Outline each uninfected red blood cell.
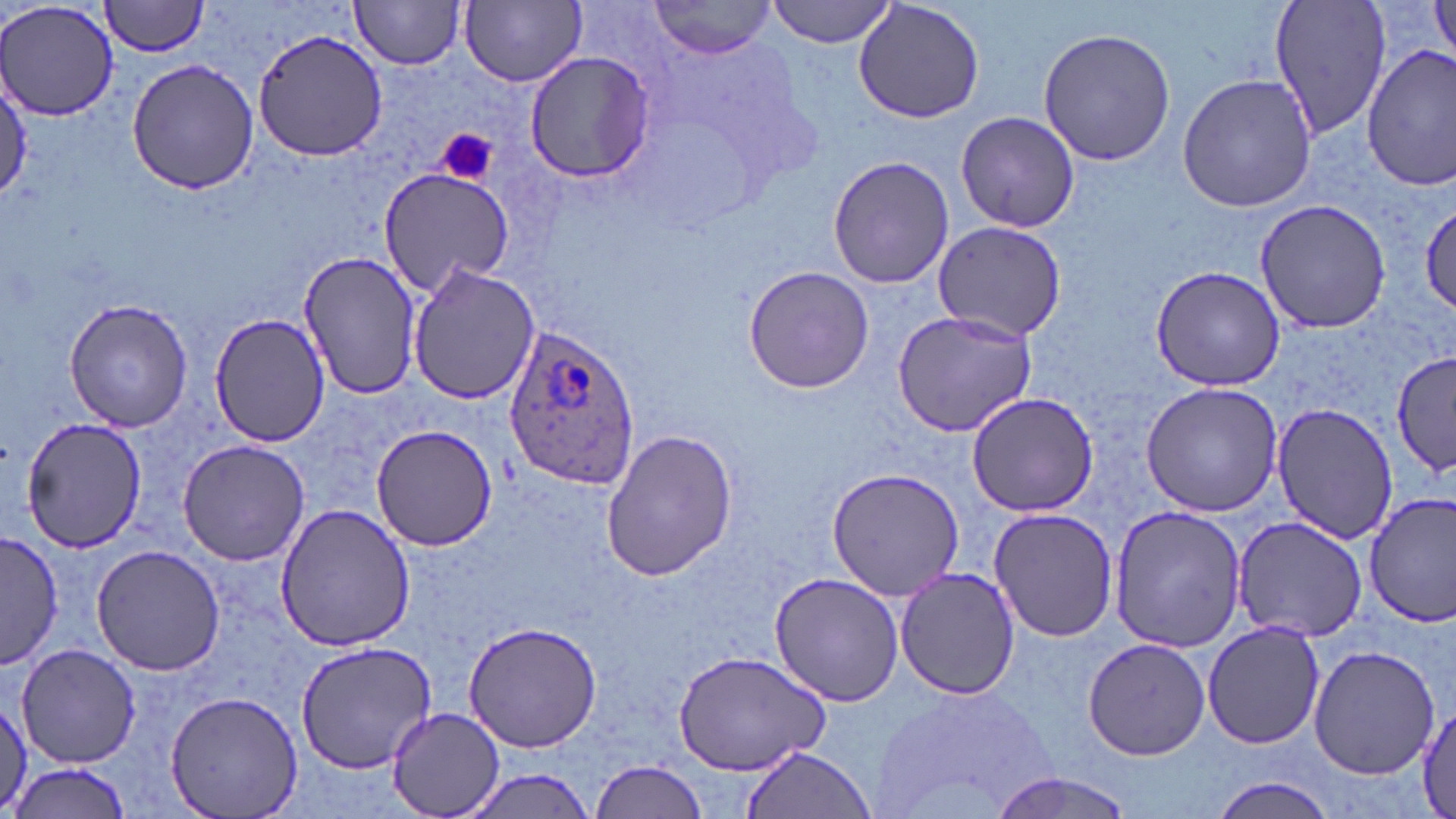
Approximate bounding boxes as (x1,y1)-(x2,y2) corner pairs in pixels.
Uninfected red blood cells: (100,0)-(213,57), (351,0)-(468,70), (766,0)-(898,48), (852,0)-(986,124), (1268,0)-(1394,146), (1427,0)-(1456,72), (0,1)-(122,119), (463,1)-(587,88), (646,1)-(777,57), (1036,25)-(1175,166), (254,28)-(389,162), (1362,46)-(1456,192), (522,50)-(659,184), (125,58)-(259,195), (0,72)-(31,203), (1176,72)-(1318,213), (956,109)-(1080,234), (826,155)-(955,288), (377,165)-(516,297), (1420,195)-(1456,318), (1255,198)-(1391,333), (933,219)-(1066,342), (296,250)-(421,400), (406,263)-(540,407), (1150,265)-(1285,391), (743,266)-(875,394), (63,298)-(196,433), (891,310)-(1039,437), (211,313)-(330,446), (1392,350)-(1456,478), (1140,381)-(1283,516), (965,393)-(1099,515), (1271,401)-(1399,547), (19,416)-(149,553), (371,424)-(497,552), (598,429)-(738,582), (177,439)-(310,566), (827,467)-(964,600), (1364,494)-(1456,626), (274,502)-(415,654), (1107,505)-(1247,653), (988,507)-(1119,643), (1232,514)-(1366,643), (2,532)-(62,670), (90,545)-(226,675), (894,567)-(1022,700), (769,571)-(905,707), (464,619)-(603,753), (1202,620)-(1328,751), (1082,637)-(1209,759), (296,640)-(440,774), (1308,643)-(1439,779), (15,644)-(142,767), (672,649)-(832,775), (870,680)-(1064,819), (0,691)-(31,813), (164,691)-(303,818), (1417,697)-(1456,816), (387,706)-(505,817), (740,747)-(875,819), (9,758)-(134,818), (591,759)-(708,819), (455,767)-(600,818), (989,772)-(1139,818), (1209,777)-(1339,819).

Plasmodium ovale-infected red blood cell locations: (502,323)-(641,490). Platelet locations: (437,129)-(497,185). Slide-level diagnosis: Plasmodium ovale. Image is 1456×819 pixels. Captured at 1000x magnification. Optical microscopy. One field of a larger specimen. Thin blood smear. May-Grünwald-Giemsa-stained preparation.